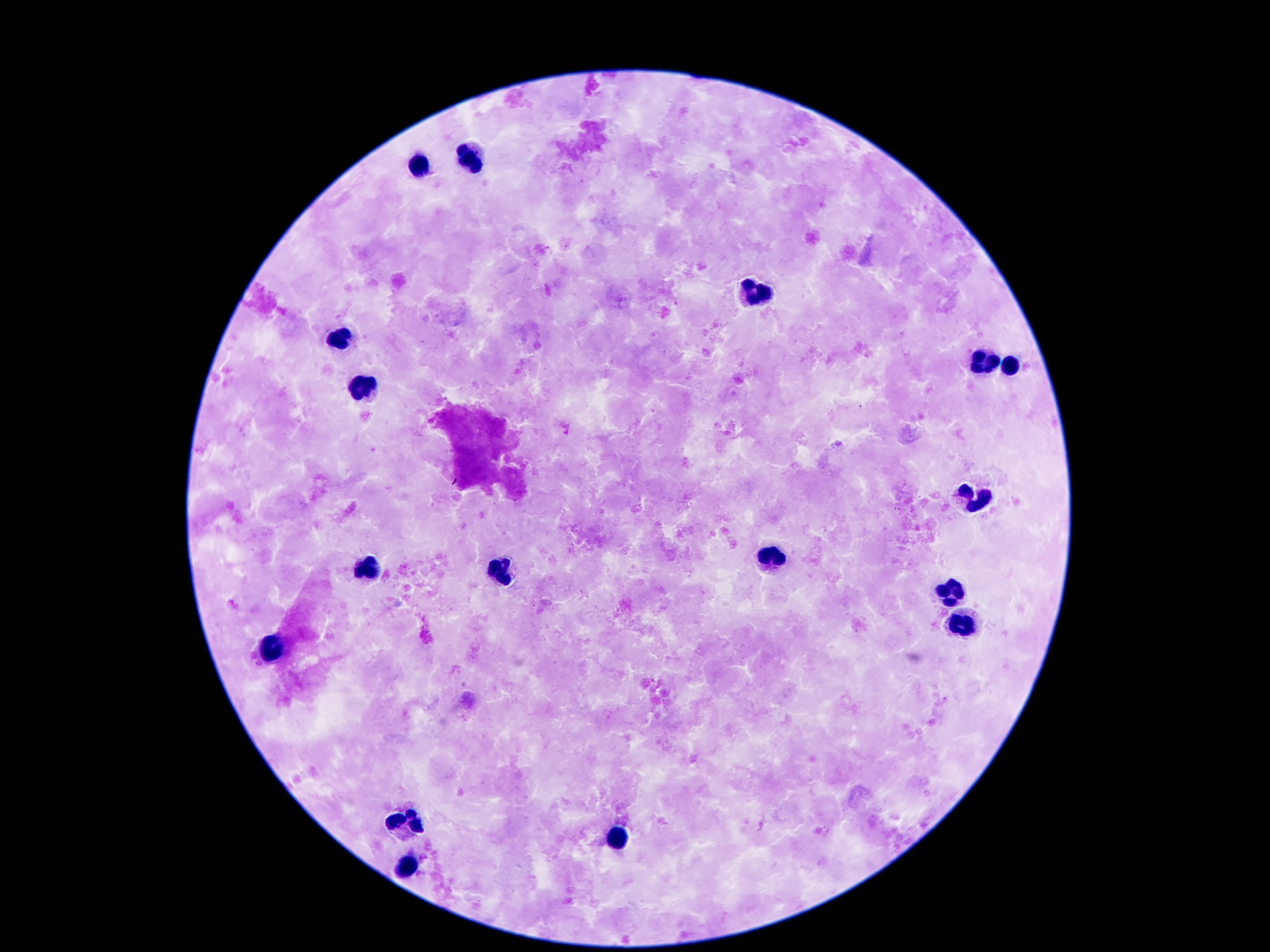
Approximate object centers, in pixels from the top-left corner. Leukocyte locations: (x=467, y=158), (x=421, y=166), (x=757, y=290), (x=339, y=339), (x=980, y=360), (x=1009, y=367), (x=361, y=390), (x=974, y=497), (x=770, y=559), (x=368, y=567), (x=503, y=571), (x=947, y=595), (x=960, y=622), (x=273, y=644), (x=410, y=825), (x=615, y=838), (x=408, y=868). Giemsa stain. Patient malaria status: uninfected. 100x magnification. Single field of view. Smartphone photograph taken through the microscope eyepiece. Image is 1270×952 pixels. Thick blood smear.